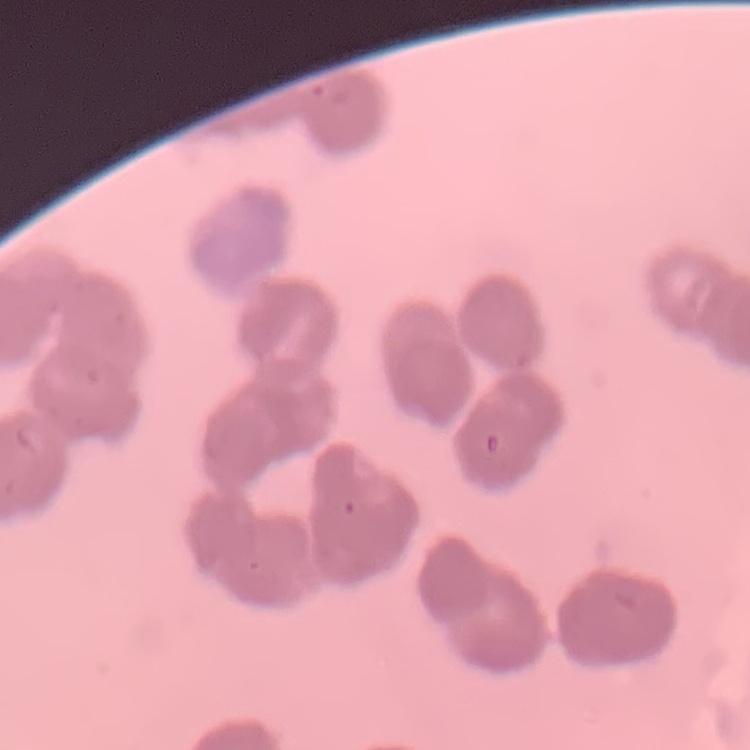
Summary:
  - Erythrocyte morphology: rouleaux formation
  - Preparation: thin blood smear
  - Image type: square crop of a larger photomicrograph
  - Stain: Field's or Giemsa